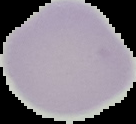

preparation = thin blood smear
malaria status = uninfected
image type = segmented cell region with the area outside set to black
image size = 136×124 pixels